Report the malaria status of this cell.
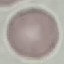
Uninfected.

{
  "image_type": "automatically extracted cell patch, resized to 64 × 64 pixels",
  "stain": "Giemsa",
  "capture": "smartphone through the microscope eyepiece",
  "preparation": "thin blood smear"
}